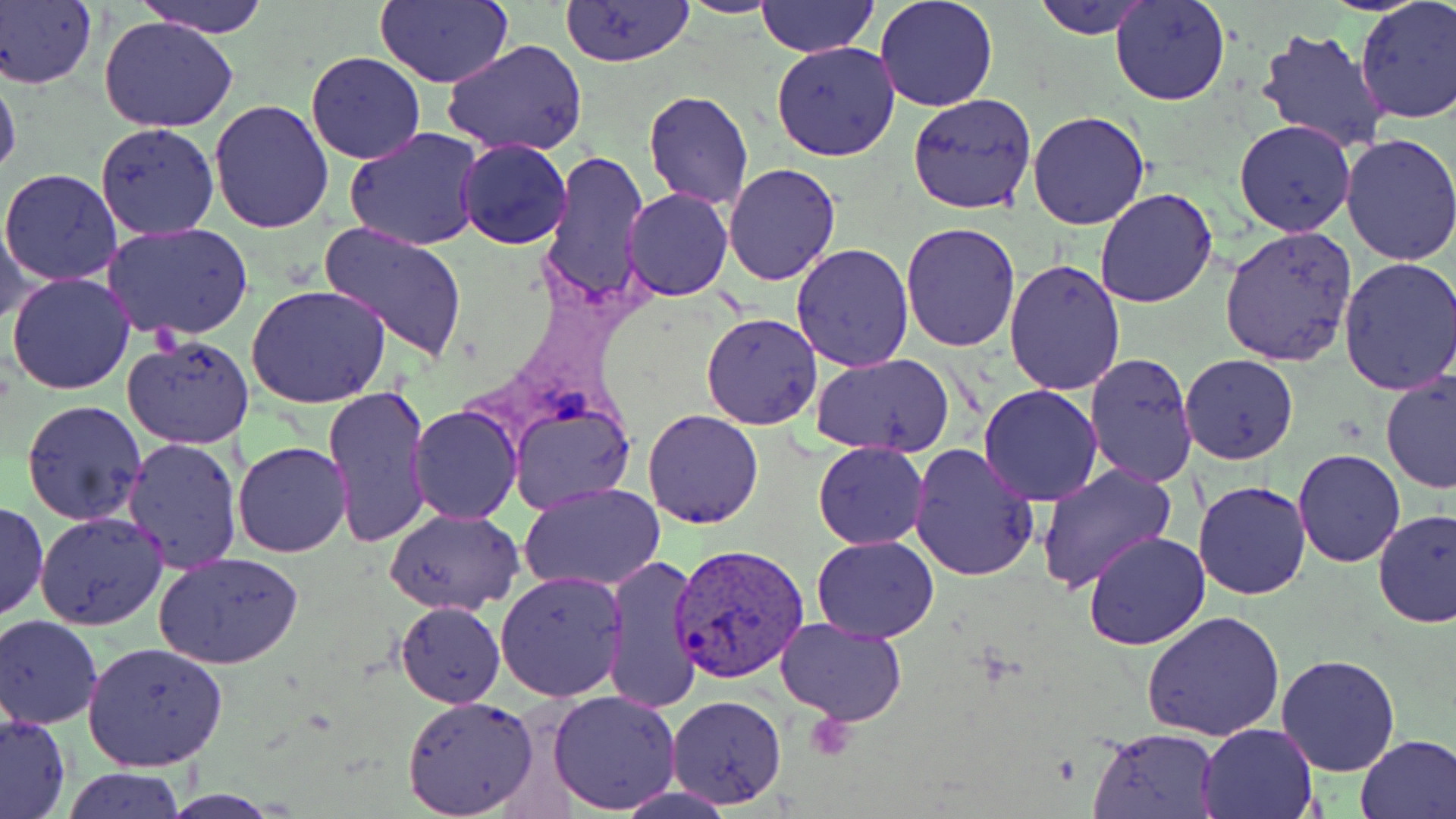
slide-level diagnosis = Plasmodium vivax
magnification = 1000x
stain = May-Grünwald-Giemsa
image size = 1456×819 pixels
preparation = thin blood smear
uninfected red blood cell locations = approximate bounding boxes as [x1, y1, x2, y2] in pixels: [132, 0, 273, 38], [377, 0, 514, 88], [559, 0, 697, 67], [675, 0, 785, 17], [757, 0, 879, 56], [875, 0, 998, 113], [1031, 0, 1155, 40], [1109, 0, 1232, 106], [0, 1, 98, 90], [1354, 1, 1456, 124], [98, 17, 241, 134], [1254, 25, 1390, 156], [886, 30, 1020, 173], [444, 38, 588, 158], [772, 41, 900, 162], [305, 52, 427, 165], [0, 73, 22, 189], [644, 90, 754, 209], [908, 93, 1037, 213], [208, 98, 336, 233], [1026, 110, 1151, 230], [1234, 119, 1358, 237], [94, 122, 219, 240], [344, 127, 484, 251], [1336, 132, 1456, 268], [457, 139, 572, 250], [542, 148, 649, 311], [722, 164, 841, 285], [1, 168, 124, 286], [622, 187, 733, 302], [1095, 188, 1219, 308], [0, 213, 36, 326], [102, 222, 253, 342], [319, 222, 469, 363], [900, 222, 1020, 354], [1219, 225, 1357, 367], [790, 242, 913, 372], [1335, 258, 1456, 395], [1004, 259, 1126, 395], [5, 273, 135, 394], [246, 285, 392, 409], [699, 312, 822, 430], [124, 335, 254, 449], [1085, 352, 1198, 489], [811, 353, 959, 456], [1179, 354, 1298, 464], [1379, 370, 1456, 493], [323, 384, 432, 547], [978, 384, 1103, 505], [22, 399, 148, 525], [508, 402, 635, 514], [408, 405, 523, 524], [642, 410, 764, 528], [120, 437, 242, 575], [232, 441, 352, 558], [811, 442, 927, 549], [908, 443, 1041, 581], [1294, 448, 1407, 567], [1036, 464, 1175, 593], [1192, 480, 1312, 600], [519, 482, 666, 595], [0, 500, 47, 623], [385, 508, 526, 616], [1372, 508, 1456, 628], [35, 511, 168, 630], [1083, 531, 1210, 650], [812, 534, 939, 643], [155, 551, 304, 668], [600, 553, 706, 716], [496, 570, 627, 703], [395, 601, 505, 708], [1141, 610, 1284, 741], [776, 615, 909, 725], [0, 616, 103, 728], [81, 642, 232, 772], [1276, 652, 1401, 775], [547, 689, 681, 814], [401, 695, 540, 818], [664, 695, 788, 809], [0, 713, 71, 819], [1196, 722, 1321, 817], [1089, 726, 1221, 818], [1354, 733, 1456, 817], [64, 767, 186, 819]
modality = light microscopy
field of view = single
Plasmodium vivax-infected red blood cell locations = approximate bounding boxes as [x1, y1, x2, y2] in pixels: [671, 542, 810, 683]